Report the malaria status of this cell.
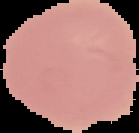

It is uninfected.

Cell region segmented out of the field of view; the surrounding area is masked to black. From a thin blood smear. Image is 139×133 pixels.